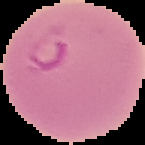
The area outside the segmented cell region is set to black. Image is 145×145 pixels. From a thin blood film. Malaria status: parasitized.